Classify this cell by malaria status.
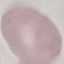
It is uninfected.

Thin blood film. Giemsa-stained preparation. Photographed with a smartphone camera at the microscope eyepiece. Automatically extracted cell patch, resized to 64 × 64 pixels.